Identify the cell.
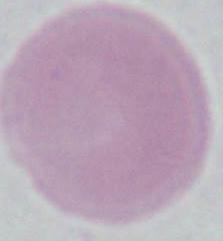

An erythrocyte.

Summary:
  - Magnification: 1000x
  - Modality: micrograph